Describe the morphology of the red blood cells.
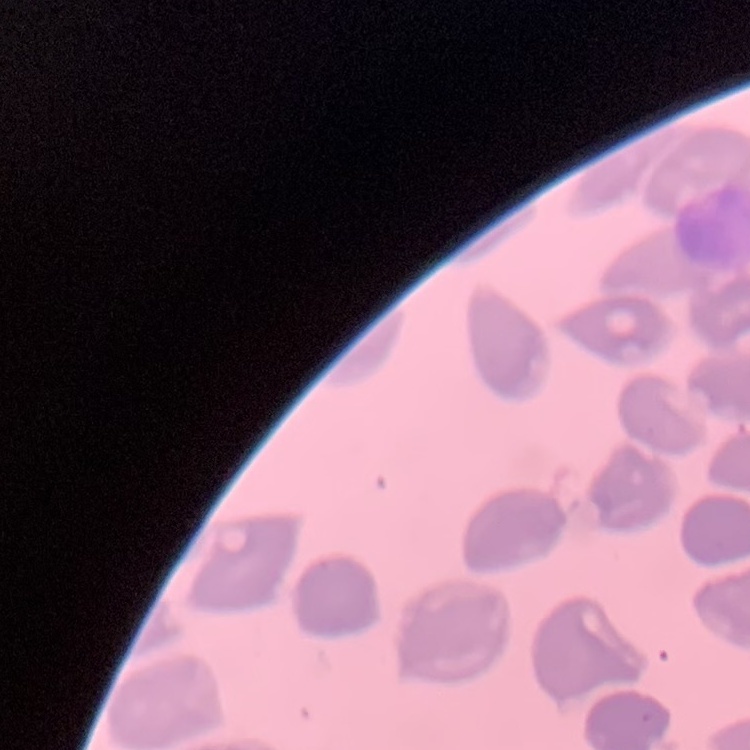
They show no rouleaux formation.

Square crop of a larger photomicrograph. Stained with either Field's or Giemsa. Thin blood film.